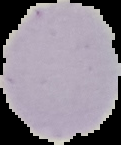

{
  "result": "no Plasmodium parasites detected",
  "image_size": "121×145 pixels",
  "image_type": "segmented cell region with the area outside set to black",
  "preparation": "thin blood smear"
}